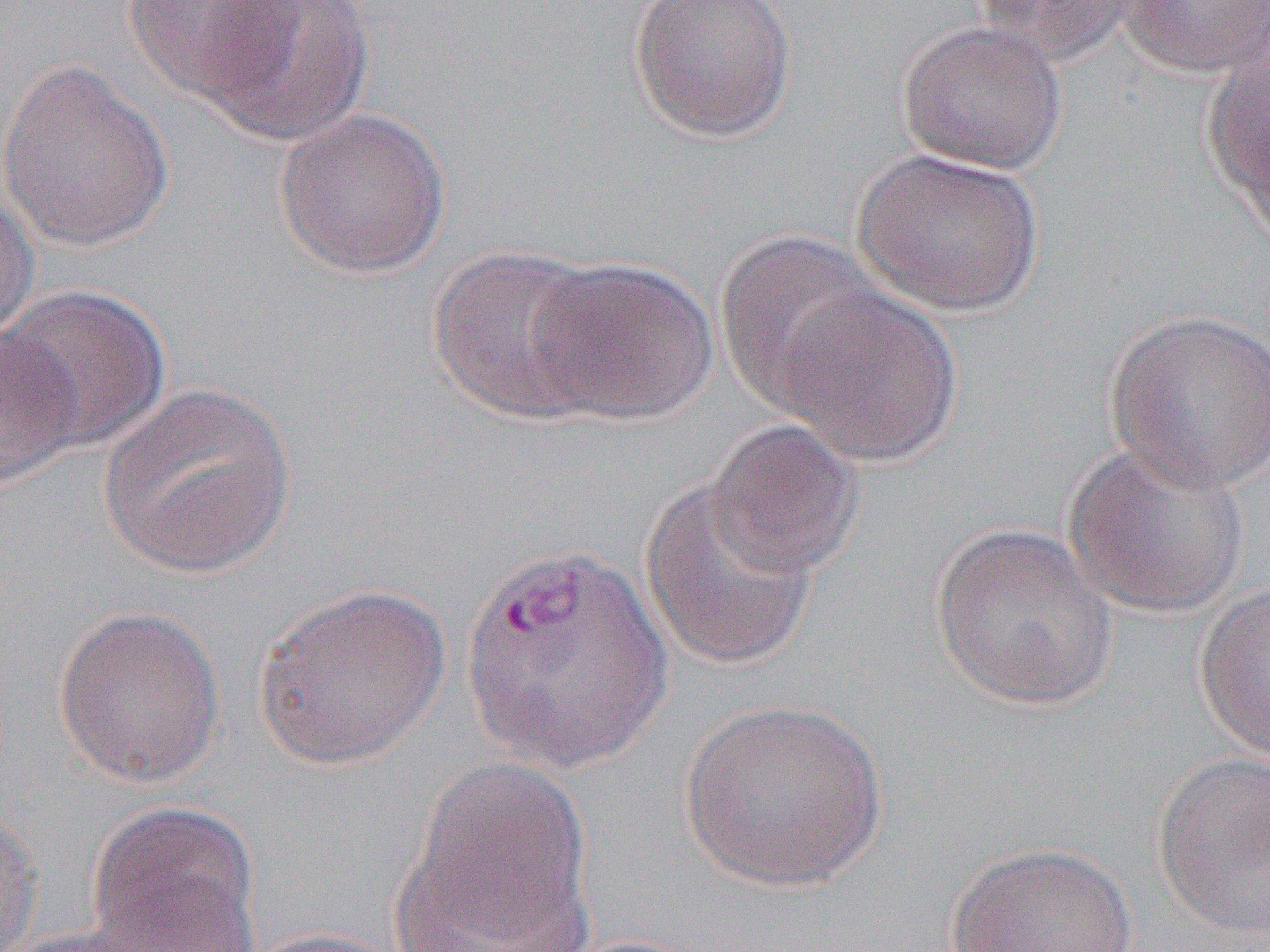

Approximate bounding boxes as named x1/y1/x2/y2 corners in pixels. Uninfected red blood cell locations: (x1=121, y1=0, x2=306, y2=108), (x1=190, y1=0, x2=381, y2=148), (x1=627, y1=0, x2=799, y2=144), (x1=964, y1=0, x2=1141, y2=66), (x1=1116, y1=0, x2=1270, y2=79), (x1=896, y1=21, x2=1069, y2=175), (x1=1199, y1=37, x2=1270, y2=230), (x1=0, y1=59, x2=174, y2=252), (x1=272, y1=108, x2=451, y2=278), (x1=851, y1=148, x2=1045, y2=318), (x1=0, y1=181, x2=40, y2=346), (x1=714, y1=232, x2=887, y2=413), (x1=427, y1=246, x2=613, y2=425), (x1=525, y1=256, x2=720, y2=426), (x1=3, y1=284, x2=171, y2=454), (x1=773, y1=285, x2=964, y2=468), (x1=1102, y1=308, x2=1270, y2=494), (x1=0, y1=328, x2=83, y2=495), (x1=97, y1=382, x2=299, y2=579), (x1=705, y1=419, x2=866, y2=580), (x1=1061, y1=440, x2=1254, y2=619), (x1=639, y1=476, x2=821, y2=673), (x1=930, y1=523, x2=1120, y2=712), (x1=1194, y1=577, x2=1270, y2=763), (x1=252, y1=581, x2=451, y2=771), (x1=53, y1=605, x2=226, y2=789), (x1=677, y1=696, x2=891, y2=893), (x1=1151, y1=751, x2=1270, y2=938), (x1=398, y1=758, x2=595, y2=949), (x1=0, y1=803, x2=41, y2=951), (x1=85, y1=804, x2=262, y2=951), (x1=944, y1=841, x2=1140, y2=951), (x1=1, y1=926, x2=171, y2=952), (x1=242, y1=927, x2=413, y2=952). Slide-level diagnosis: Plasmodium vivax. Single field of view. Thin blood smear. 1000x magnification. Image is 1270×952 pixels. Optical microscopy.